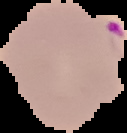

image type = segmented cell region on a black background
image size = 127×133 pixels
preparation = thin blood smear
malaria status = parasitized